Classify this cell by malaria status.
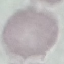

It is uninfected.

Giemsa-stained preparation. Cell patch, automatically extracted from a larger field of view and resized to 64 × 64 pixels. Thin smear of blood. Acquired by smartphone through the microscope eyepiece.